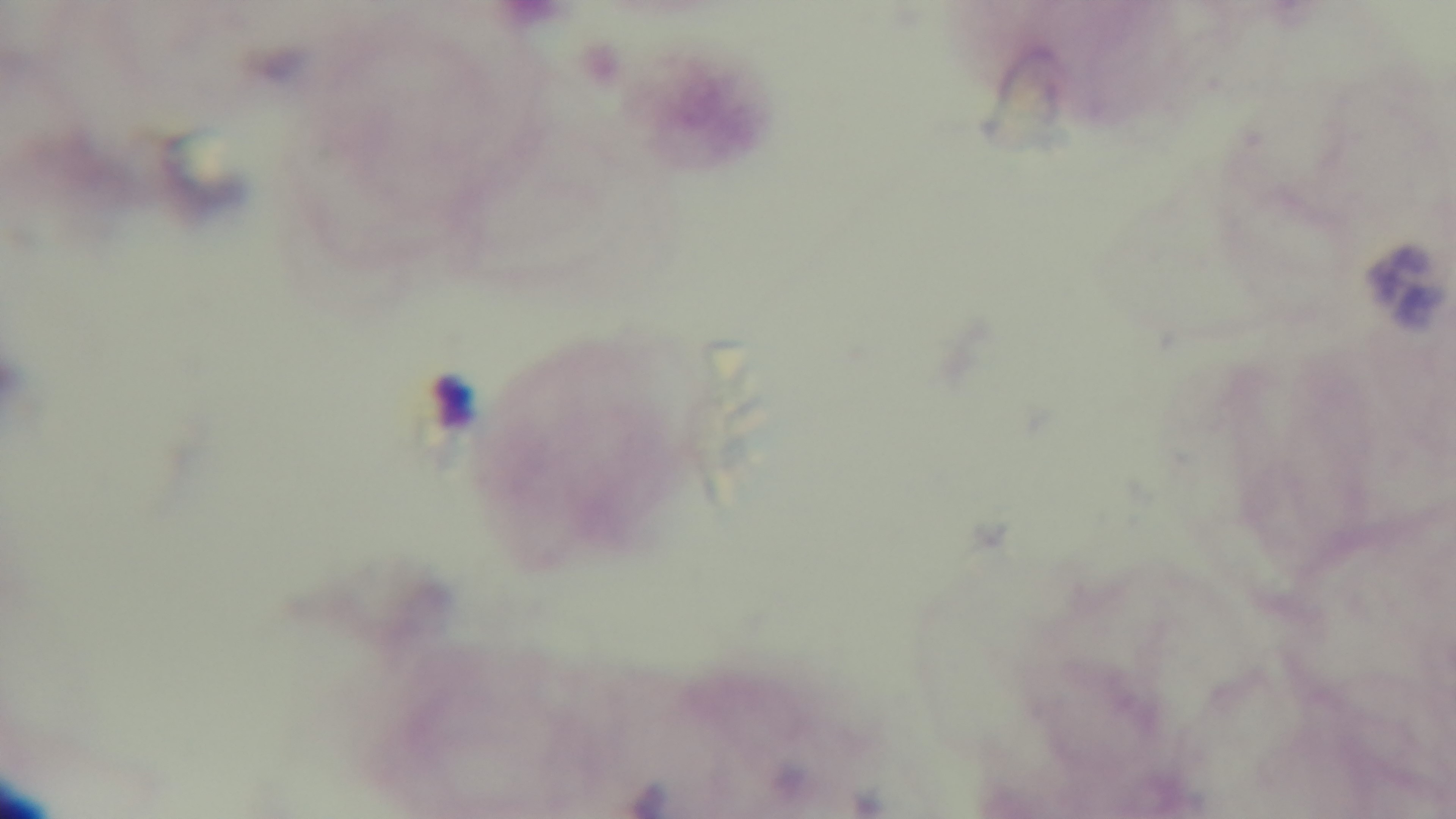

One field from the slide. Photomicrograph. Giemsa stain. 100x oil-immersion objective. Malaria status: uninfected. Mounted 4K digital camera. Preparation: thick smear.